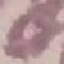
result = no malaria parasites seen
capture = smartphone camera at the microscope eyepiece
image type = cell patch, automatically extracted from a larger field of view and resized to 64 × 64 pixels
stain = Giemsa
preparation = thin blood smear